Describe the morphology of the erythrocytes.
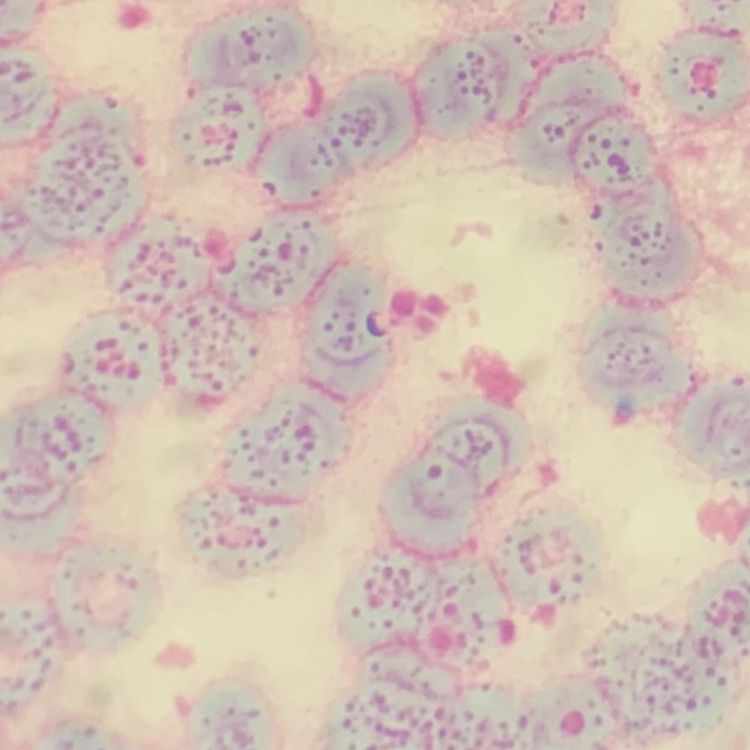
They show rouleaux formation.

stain = Field's or Giemsa
preparation = thin peripheral smear
image type = square crop of a larger photomicrograph